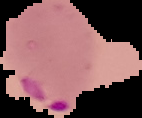
image type = cell region segmented out of the field of view; surrounding area masked to black
preparation = thin blood film
image size = 142×118 pixels
result = Plasmodium parasites detected